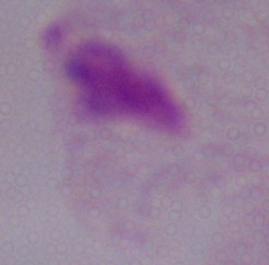

Summary:
  - Magnification: 1000x
  - Identification: trichomonad
  - Modality: photomicrograph